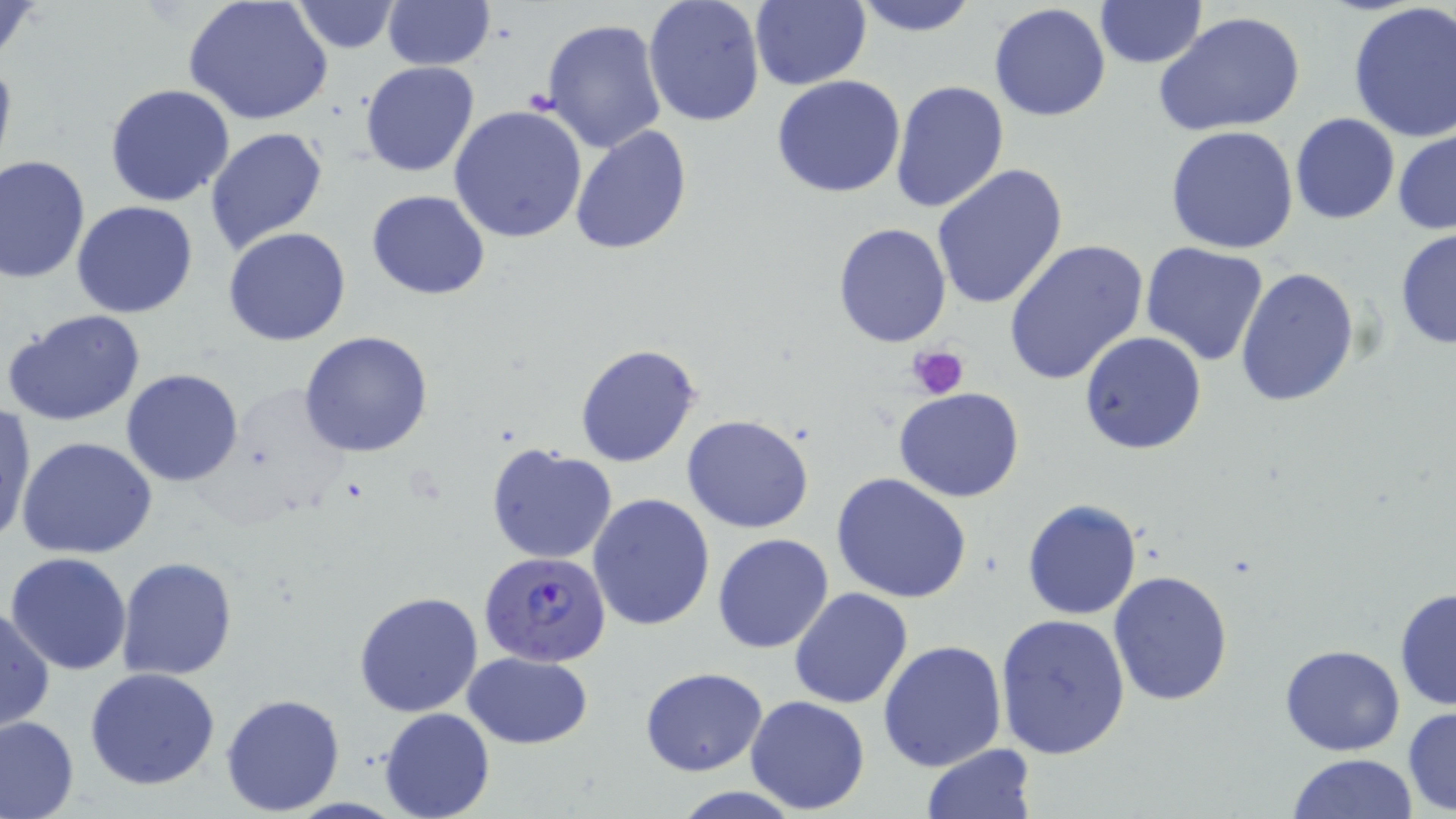

slide-level diagnosis = Plasmodium falciparum
magnification = 1000x
image size = 1456×819 pixels
stain = May-Grünwald-Giemsa
preparation = thin blood smear
uninfected red blood cell locations = approximate bounding boxes as (x1,y1)-(x2,y2) corner pairs in pixels: (0,0)-(45,69), (382,0)-(494,71), (750,0)-(871,91), (848,0)-(983,38), (183,1)-(334,125), (288,1)-(402,54), (642,1)-(765,126), (1094,1)-(1207,69), (989,2)-(1112,122), (1347,2)-(1456,144), (1154,12)-(1306,139), (540,19)-(668,155), (0,46)-(17,181), (358,60)-(480,177), (770,74)-(906,198), (890,79)-(1009,216), (104,83)-(236,206), (448,106)-(589,246), (1290,113)-(1399,224), (203,125)-(329,254), (568,125)-(693,255), (1165,125)-(1299,254), (1392,126)-(1456,236), (0,155)-(91,284), (932,163)-(1068,310), (367,190)-(490,300), (71,200)-(197,318), (832,222)-(953,349), (223,228)-(352,346), (1393,228)-(1456,349), (1004,238)-(1149,386), (1139,241)-(1272,367), (1235,266)-(1361,409), (3,307)-(147,427), (1079,331)-(1208,455), (300,332)-(434,458), (574,344)-(701,468), (121,368)-(244,486), (893,387)-(1024,502), (0,403)-(37,547), (683,414)-(815,533), (17,434)-(158,559), (485,445)-(618,566), (830,474)-(972,606), (586,493)-(714,632), (1023,499)-(1142,621), (713,534)-(835,655), (5,552)-(134,675), (116,556)-(237,681), (1107,569)-(1235,706), (789,588)-(914,710), (1393,588)-(1455,711), (354,590)-(484,719), (0,602)-(53,733), (996,614)-(1130,761), (877,640)-(1008,774), (1279,644)-(1405,755), (462,650)-(592,749), (84,666)-(221,790), (641,667)-(767,776), (221,692)-(346,814), (744,695)-(871,813), (1402,706)-(1456,815), (379,708)-(494,819), (0,715)-(78,818), (921,744)-(1037,818), (1287,753)-(1421,818)
Plasmodium falciparum-infected red blood cell locations = approximate bounding boxes as (x1,y1)-(x2,y2) corner pairs in pixels: (480,550)-(612,668)
platelet locations = approximate bounding boxes as (x1,y1)-(x2,y2) corner pairs in pixels: (908,344)-(969,402)
field of view = one of a larger specimen
modality = optical microscopy